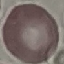

result: no malaria parasites detected
image_type: cell patch, automatically extracted from a larger field of view and resized to 64 × 64 pixels
capture: smartphone through the microscope eyepiece
stain: Giemsa
preparation: thin blood smear